Classify this cell by malaria status.
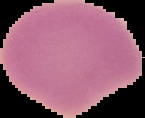
Uninfected.

Summary:
  - Image size: 145×118 pixels
  - Image type: segmented cell region on a black background
  - Preparation: thin blood film